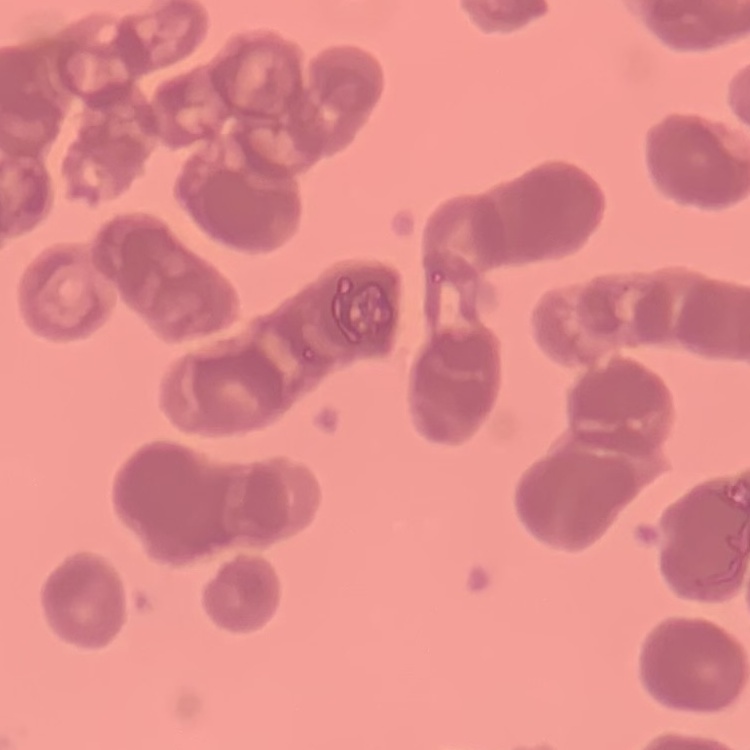
Summary:
  - Erythrocyte morphology: rouleaux formation
  - Preparation: thin peripheral smear
  - Image type: square crop of a larger photomicrograph
  - Stain: Field's or Giemsa